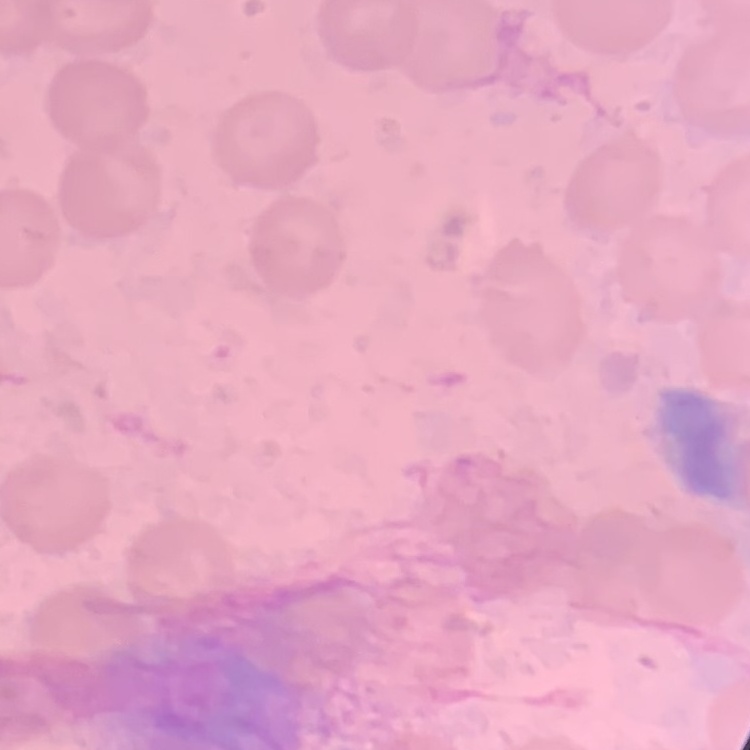

The red blood cells exhibit no rouleaux formation. Thin blood film. Square crop of a larger photomicrograph. Field's or Giemsa stain.